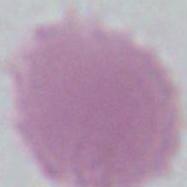

Captured at 1000x magnification. Photomicrograph. An erythrocyte is shown.